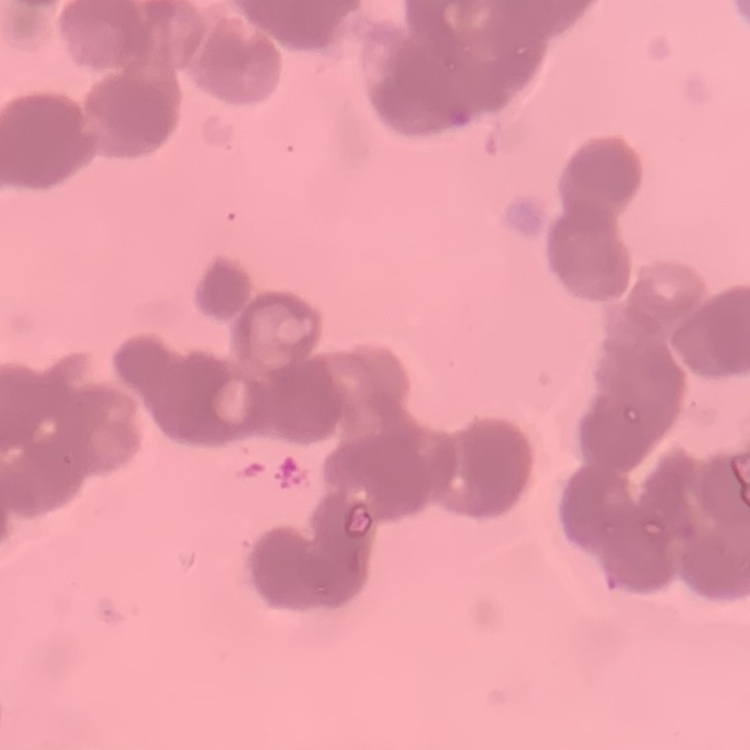

Summary:
  - Erythrocyte morphology: rouleaux formation
  - Preparation: thin blood smear
  - Stain: Field's or Giemsa
  - Image type: one tile cut from a larger photomicrograph